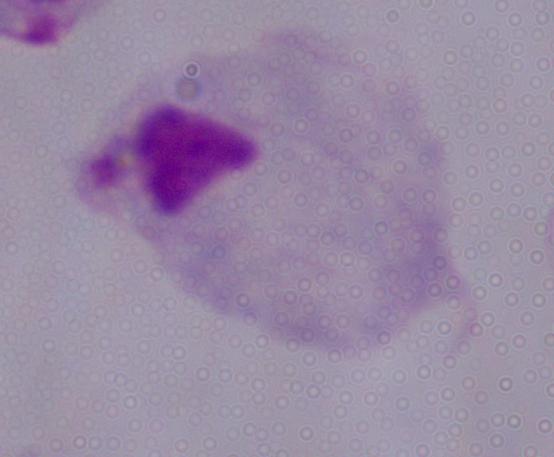

modality = micrograph
identification = trichomonad
magnification = 1000x